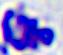 Captured at 400x magnification. Micrograph. A leukocyte is shown.